Assess this cell for malaria.
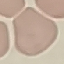
It is uninfected.

Thin blood smear. Giemsa stain. Automatically extracted cell patch, resized to 64 × 64 pixels. Acquired by smartphone through the microscope eyepiece.